Outline each P. falciparum parasite and classify it by life-cycle stage.
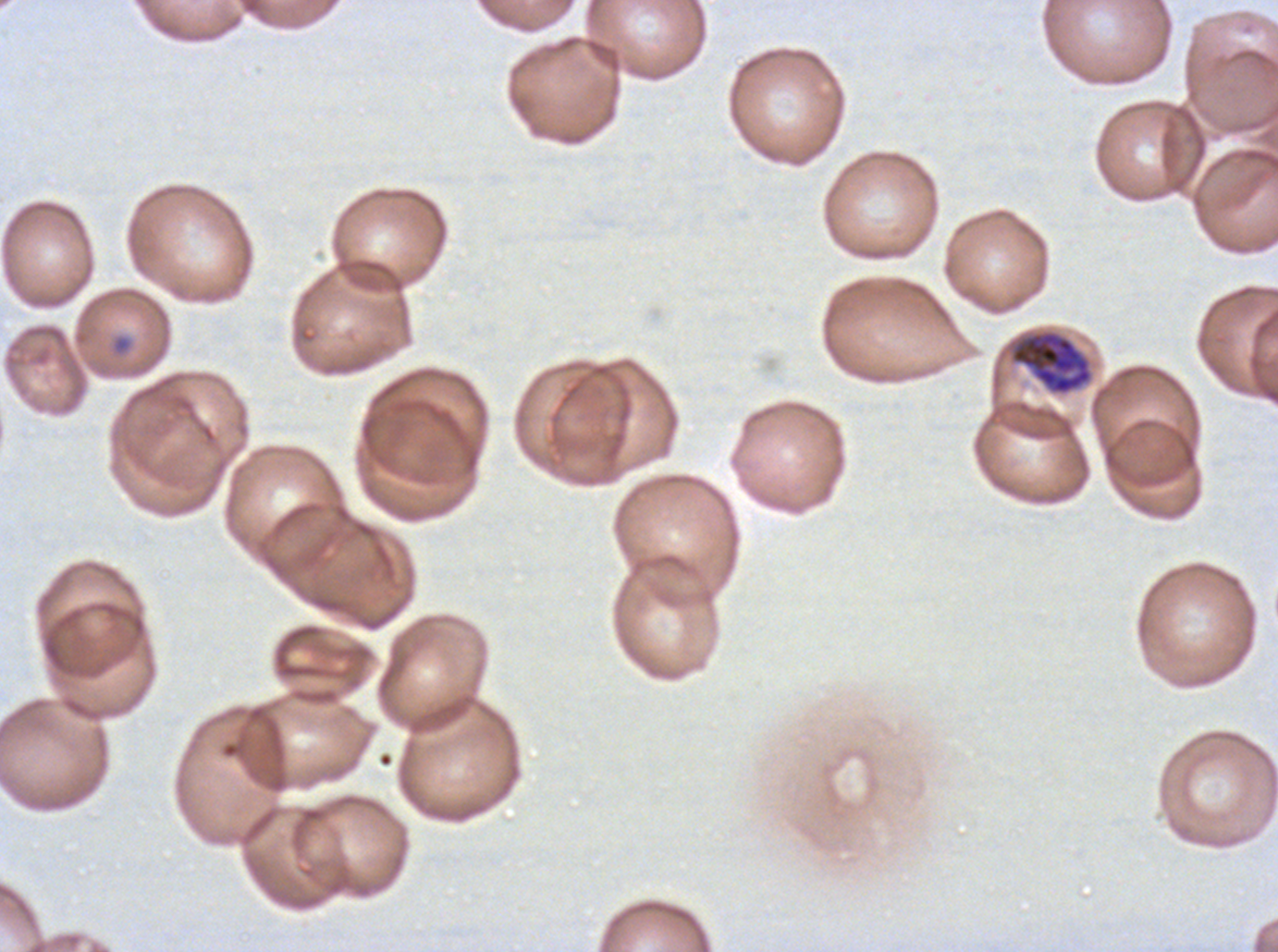

Approximate bounding rectangles given as corner coordinates in pixels from the top-left.
Rings: (x1=112, y1=335, x2=132, y2=354).
Late trophozoites: (x1=1010, y1=330, x2=1093, y2=396).
No late-ring/early-trophozoite forms, mid trophozoites, early schizonts, late schizonts, segmenters, or gametocytes observed.

P. falciparum cultured ex vivo for 24 to 48 hours, from a patient in The Gambia. One sub-image of a larger composite. Giemsa stain. Image is 1278×952 pixels. Life-cycle stages observed: ring, late trophozoite. Thin blood smear.